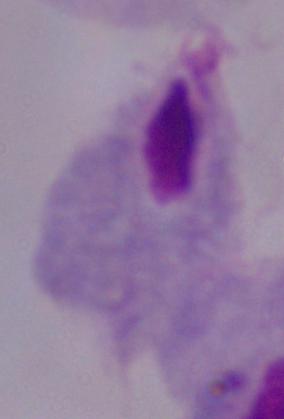 Photomicrograph. 1000x magnification. A trichomonad is seen.